Name the parasite shown.
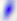

This is Toxoplasma gondii.

400x magnification. Photomicrograph.